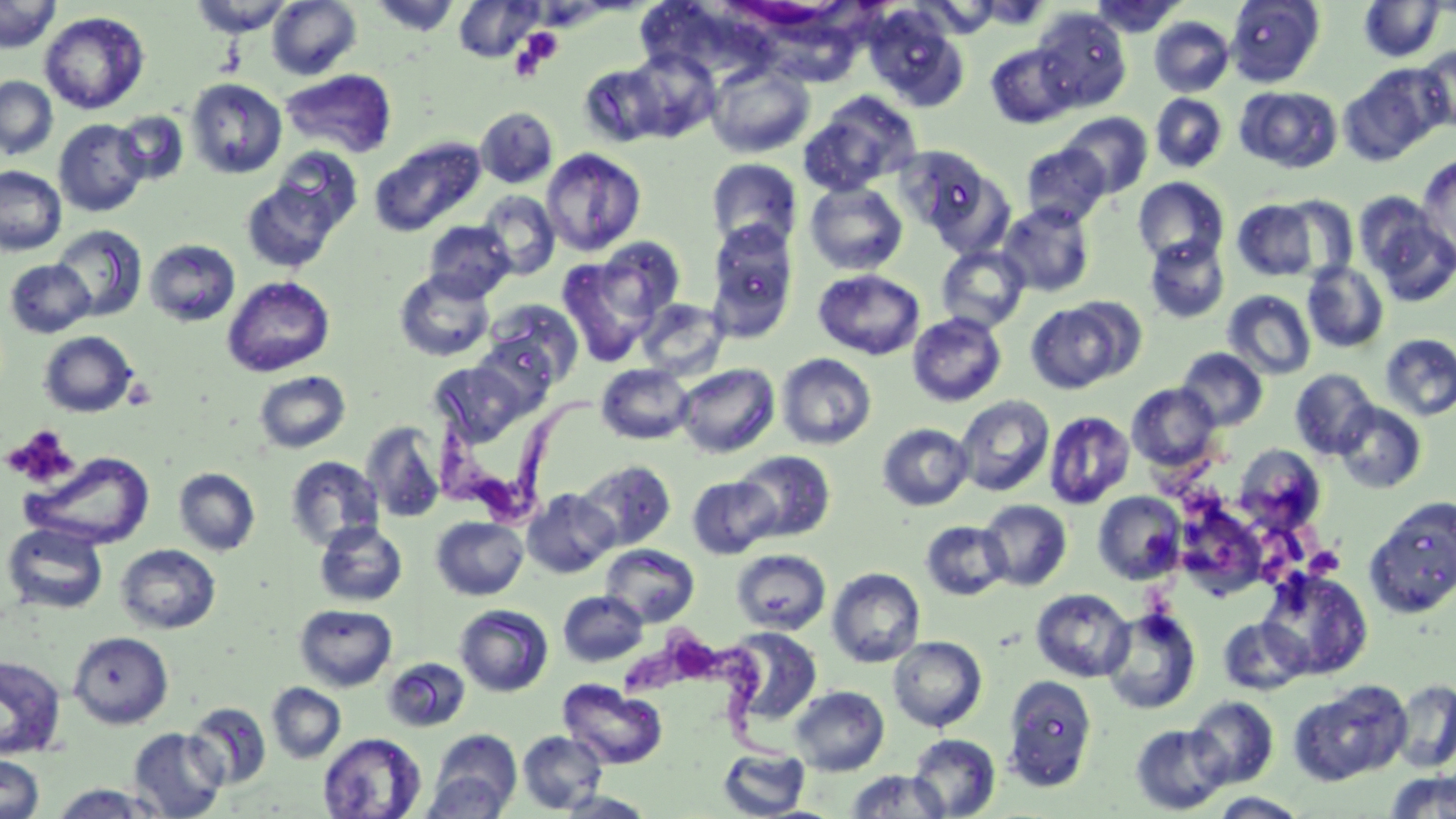

slide-level diagnosis = Trypanosoma brucei
uninfected red blood cell locations = approximate bounding boxes as (x1,y1)-(x2,y2) corner pairs in pixels: (0,0)-(59,53), (189,0)-(294,37), (267,0)-(362,80), (370,0)-(460,36), (1090,0)-(1186,38), (1226,0)-(1325,87), (1358,0)-(1445,61), (454,1)-(541,62), (863,6)-(968,111), (1032,7)-(1132,111), (39,11)-(149,114), (1149,17)-(1235,97), (984,43)-(1077,128), (1416,45)-(1456,133), (706,62)-(815,158), (1340,68)-(1445,164), (280,70)-(397,158), (0,76)-(58,160), (187,78)-(286,179), (1236,86)-(1343,173), (1151,93)-(1228,173), (797,106)-(915,196), (475,107)-(558,187), (1059,112)-(1153,198), (113,113)-(189,185), (53,119)-(150,217), (370,137)-(486,237), (1019,143)-(1110,228), (894,146)-(994,235), (541,148)-(646,256), (1416,153)-(1456,264), (705,158)-(803,251), (0,165)-(66,256), (1133,177)-(1229,266), (239,178)-(343,272), (805,181)-(909,275), (477,190)-(560,280), (1277,196)-(1358,279), (1232,200)-(1319,281), (996,202)-(1096,297), (1361,203)-(1456,307), (423,220)-(516,302), (707,222)-(799,340), (51,225)-(147,321), (1144,235)-(1230,324), (595,237)-(686,323), (144,239)-(240,326), (936,245)-(1030,333), (558,256)-(656,366), (4,259)-(95,338), (1302,261)-(1389,353), (394,269)-(495,361), (814,269)-(924,360), (222,276)-(335,377), (1223,290)-(1316,380), (484,298)-(584,388), (636,298)-(728,379), (1025,301)-(1131,394), (908,312)-(1006,407), (38,330)-(138,417), (1379,333)-(1456,421), (1176,348)-(1268,431), (776,353)-(877,450), (429,360)-(534,446), (674,363)-(780,458), (596,364)-(694,445), (1290,368)-(1379,459), (253,370)-(351,453), (1127,382)-(1221,472), (955,395)-(1054,497), (1333,402)-(1426,494), (1044,410)-(1135,509), (361,422)-(446,523), (877,423)-(973,510), (1233,444)-(1325,533), (23,451)-(155,549), (733,451)-(835,542), (285,456)-(385,551), (577,460)-(677,550), (174,468)-(260,556), (687,475)-(778,559), (521,488)-(619,578), (1093,491)-(1186,584), (1174,498)-(1269,598), (978,499)-(1072,590), (1363,499)-(1456,618), (431,516)-(528,599), (314,520)-(407,607), (920,521)-(1011,600), (2,522)-(108,614), (116,544)-(221,634), (600,544)-(699,627), (731,549)-(831,635), (827,567)-(925,667), (1256,567)-(1373,680), (1031,588)-(1134,681), (558,590)-(648,667), (295,603)-(397,691), (454,604)-(554,697), (1101,607)-(1201,715), (1218,617)-(1311,695), (723,626)-(822,726), (69,631)-(173,728), (888,636)-(987,731), (0,655)-(67,760), (383,658)-(471,731), (1002,675)-(1098,791), (559,679)-(667,769), (1389,679)-(1456,773), (1288,680)-(1411,785), (267,683)-(346,763), (790,685)-(890,776), (1187,696)-(1279,788), (186,702)-(271,789), (1130,723)-(1231,814), (128,727)-(227,818), (428,728)-(523,815), (517,731)-(608,813), (318,732)-(426,819), (908,733)-(1001,818), (717,746)-(811,818), (0,754)-(45,819), (422,770)-(513,819), (843,770)-(949,818), (1384,770)-(1456,818), (49,784)-(166,818), (556,790)-(655,818), (1207,792)-(1310,818)
modality = light microscopy
magnification = 1000x
field of view = single
preparation = thin blood smear
stain = May-Grünwald-Giemsa
Trypanosoma brucei locations = approximate bounding boxes as (x1,y1)-(x2,y2) corner pairs in pixels: (433,376)-(619,519), (619,633)-(804,774)
platelet locations = approximate bounding boxes as (x1,y1)-(x2,y2) corner pairs in pixels: (520,28)-(562,67), (509,38)-(551,81), (3,425)-(80,489), (1305,546)-(1346,577)
image size = 1456×819 pixels